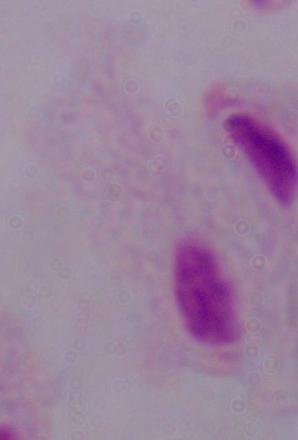 1000x magnification. Photomicrograph. A trichomonad is seen.